Locate the cells, classifying each as a parasitized red blood cell, an uninfected red blood cell, or a white blood cell.
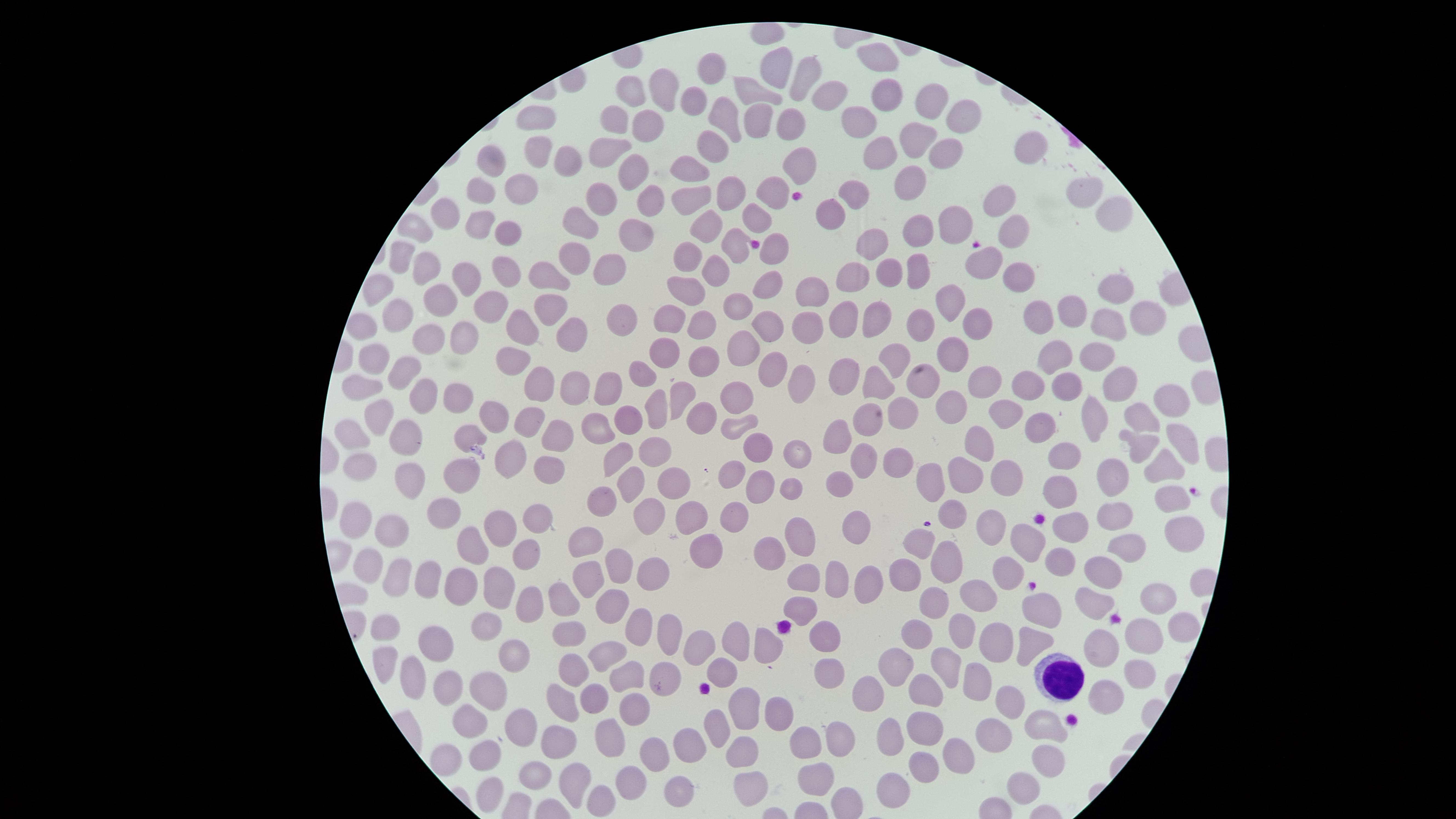
No parasitized red blood cells identified.
Approximate marker points as {x, y} in pixels.
Uninfected red blood cells: {877, 59}, {780, 69}, {709, 70}, {806, 74}, {665, 85}, {634, 92}, {749, 92}, {883, 96}, {829, 97}, {692, 101}, {929, 108}, {724, 115}, {539, 116}, {612, 117}, {965, 117}, {855, 119}, {756, 121}, {643, 123}, {785, 125}, {915, 138}, {710, 148}, {882, 152}, {938, 152}, {601, 153}, {538, 154}, {1031, 155}, {630, 162}, {569, 163}, {492, 164}, {691, 167}, {798, 169}, {908, 181}, {479, 192}, {735, 192}, {519, 193}, {1081, 193}, {772, 194}, {599, 195}, {640, 198}, {855, 200}, {688, 202}, {1002, 204}, {832, 211}, {1106, 211}, {445, 215}, {581, 218}, {756, 219}, {478, 220}, {702, 224}, {952, 226}, {1009, 230}, {504, 231}, {417, 233}, {915, 233}, {628, 234}, {738, 244}, {874, 244}, {774, 252}, {688, 253}, {401, 254}, {572, 258}, {604, 262}, {424, 265}, {914, 267}, {985, 267}, {713, 270}, {1015, 273}, {464, 274}, {853, 274}, {889, 275}, {500, 276}, {543, 276}, {767, 284}, {376, 285}, {686, 286}, {1110, 288}, {812, 297}, {446, 301}, {946, 303}, {486, 305}, {548, 308}, {740, 309}, {1068, 312}, {845, 315}, {395, 316}, {881, 316}, {1145, 316}, {670, 317}, {699, 320}, {1039, 320}, {623, 321}, {362, 322}, {521, 325}, {763, 326}, {975, 326}, {1108, 326}, {808, 327}, {917, 330}, {424, 337}, {457, 337}, {568, 338}, {742, 348}, {663, 350}, {958, 352}, {1052, 352}, {374, 356}, {1086, 357}, {895, 359}, {702, 360}, {507, 363}, {407, 367}, {765, 367}, {845, 371}, {638, 377}, {983, 379}, {879, 381}, {920, 381}, {1060, 381}, {535, 382}, {800, 382}, {1115, 382}, {575, 383}, {1033, 383}, {363, 387}, {609, 388}, {427, 391}, {738, 395}, {460, 396}, {683, 396}, {1168, 399}, {947, 409}, {649, 410}, {1005, 414}, {495, 415}, {635, 415}, {380, 417}, {1089, 417}, {699, 418}, {904, 418}, {532, 419}, {863, 421}, {1145, 421}, {737, 424}, {598, 427}, {1044, 428}, {356, 431}, {406, 431}, {468, 435}, {558, 436}, {839, 436}, {1179, 437}, {756, 443}, {973, 443}, {1135, 445}, {621, 452}, {796, 453}, {656, 454}, {901, 457}, {1069, 457}, {507, 460}, {863, 460}, {1164, 464}, {364, 470}, {548, 473}, {729, 475}, {933, 475}, {969, 475}, {461, 479}, {1005, 479}, {407, 482}, {674, 482}, {844, 482}, {1112, 482}, {763, 483}, {794, 486}, {632, 487}, {600, 493}, {1062, 494}, {1170, 497}, {445, 512}, {956, 512}, {1116, 514}, {646, 516}, {733, 516}, {683, 517}, {355, 521}, {994, 522}, {537, 526}, {1077, 527}, {500, 528}, {858, 528}, {390, 531}, {1185, 532}, {801, 540}, {586, 542}, {1035, 542}, {919, 545}, {475, 546}, {703, 546}, {1128, 548}, {526, 554}, {768, 554}, {944, 559}, {365, 565}, {1065, 566}, {619, 567}, {1012, 570}, {650, 572}, {907, 574}, {1105, 574}, {396, 576}, {590, 576}, {809, 577}, {423, 578}, {839, 578}, {454, 584}, {868, 588}, {504, 594}, {978, 594}, {1158, 596}, {564, 600}, {936, 604}, {1091, 604}, {614, 606}, {801, 608}, {1039, 608}, {530, 609}, {386, 624}, {1178, 625}, {638, 626}, {486, 627}, {673, 630}, {965, 631}, {915, 632}, {1141, 632}, {567, 635}, {825, 638}, {1029, 639}, {436, 640}, {701, 642}, {769, 642}, {996, 642}, {739, 643}, {1095, 645}, {608, 654}, {385, 657}, {950, 660}, {515, 661}, {897, 663}, {575, 667}, {721, 667}, {825, 668}, {664, 670}, {1137, 671}, {629, 674}, {416, 677}, {978, 681}, {452, 689}, {489, 690}, {923, 690}, {868, 692}, {562, 699}, {591, 699}, {1107, 700}, {1009, 703}, {741, 705}, {632, 706}, {781, 712}, {466, 720}, {715, 723}, {919, 723}, {526, 727}, {1045, 729}, {888, 732}, {988, 732}, {611, 738}, {841, 739}, {804, 742}, {561, 744}, {686, 744}, {744, 752}, {656, 753}, {959, 757}, {1044, 757}, {483, 759}, {446, 760}, {928, 766}, {811, 771}, {634, 776}, {538, 778}, {572, 781}, {890, 782}, {1025, 782}, {751, 784}, {679, 788}, {483, 793}, {602, 797}.
White blood cells: {1062, 679}.

Giemsa stain. The visible region is circular. Image is 1456×819 pixels. Photographed with a smartphone camera through the microscope eyepiece. Thin blood smear. One field of view of the specimen.